Give the extent of all Plasmodium ovale-infected red blood cells.
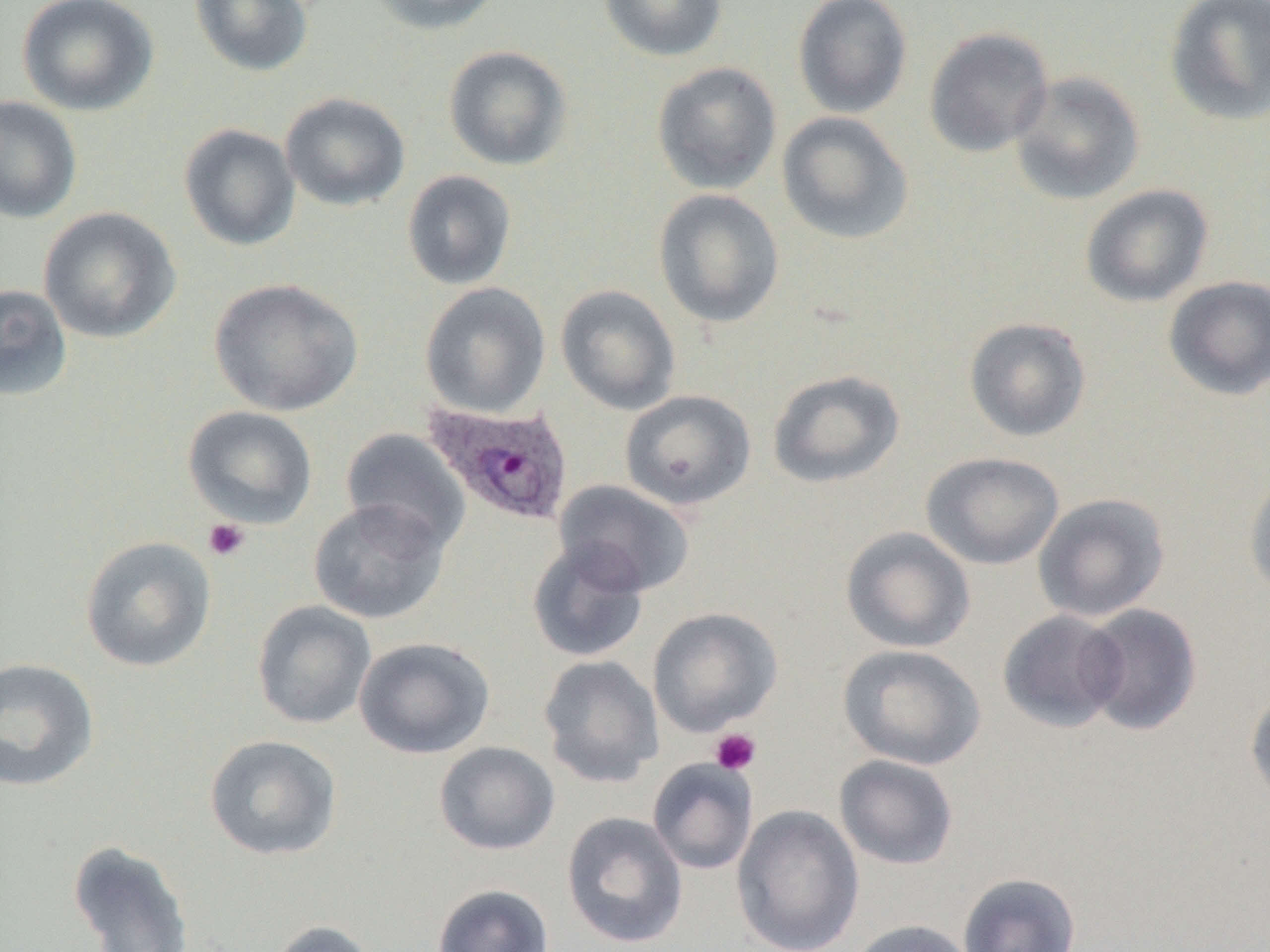
Approximate bounding boxes as (x1, y1, x2, y2) in pixels.
Plasmodium ovale-infected red blood cells: (422, 400, 576, 527).

slide-level diagnosis = Plasmodium ovale
modality = optical microscopy
image size = 1270×952 pixels
magnification = 1000x
field of view = one of a larger specimen
preparation = thin blood smear
platelet locations = approximate bounding boxes as (x1, y1, x2, y2) in pixels: (203, 518, 251, 562), (709, 728, 762, 775)
uninfected red blood cell locations = approximate bounding boxes as (x1, y1, x2, y2) in pixels: (16, 0, 160, 116), (189, 0, 315, 77), (363, 0, 507, 35), (598, 0, 728, 62), (792, 0, 913, 118), (1164, 0, 1270, 126), (923, 27, 1054, 157), (443, 45, 573, 171), (651, 61, 782, 195), (1009, 71, 1145, 205), (280, 92, 410, 212), (0, 95, 82, 224), (777, 112, 915, 245), (179, 123, 301, 251), (401, 170, 517, 290), (1080, 184, 1214, 308), (652, 188, 785, 328), (37, 206, 182, 344), (1163, 275, 1270, 401), (208, 278, 363, 416), (420, 282, 551, 418), (0, 283, 73, 402), (555, 285, 681, 415), (964, 316, 1092, 442), (767, 369, 906, 489), (620, 389, 756, 511), (182, 406, 318, 529), (340, 428, 471, 552), (920, 451, 1065, 570), (1243, 468, 1270, 603), (554, 480, 695, 597), (1033, 492, 1171, 622), (308, 498, 450, 624), (840, 526, 976, 653), (79, 536, 217, 672), (526, 539, 650, 662), (251, 600, 377, 729), (1079, 603, 1203, 736), (647, 607, 783, 736), (997, 609, 1127, 733), (354, 637, 496, 759), (837, 644, 986, 770), (537, 654, 664, 788), (0, 656, 100, 793), (1245, 686, 1270, 811), (204, 734, 343, 861), (434, 741, 560, 855), (834, 754, 959, 870), (647, 758, 759, 875), (731, 804, 865, 952), (560, 810, 688, 949), (68, 840, 195, 952), (958, 872, 1082, 952), (431, 883, 554, 952), (265, 919, 380, 952), (845, 919, 978, 952)